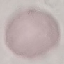

Result: no malaria parasites seen. Automatically extracted cell patch, resized to 64 × 64 pixels. Photographed with a smartphone camera at the microscope eyepiece. Thin smear of blood. Giemsa-stained preparation.